Describe the morphology of the red blood cells.
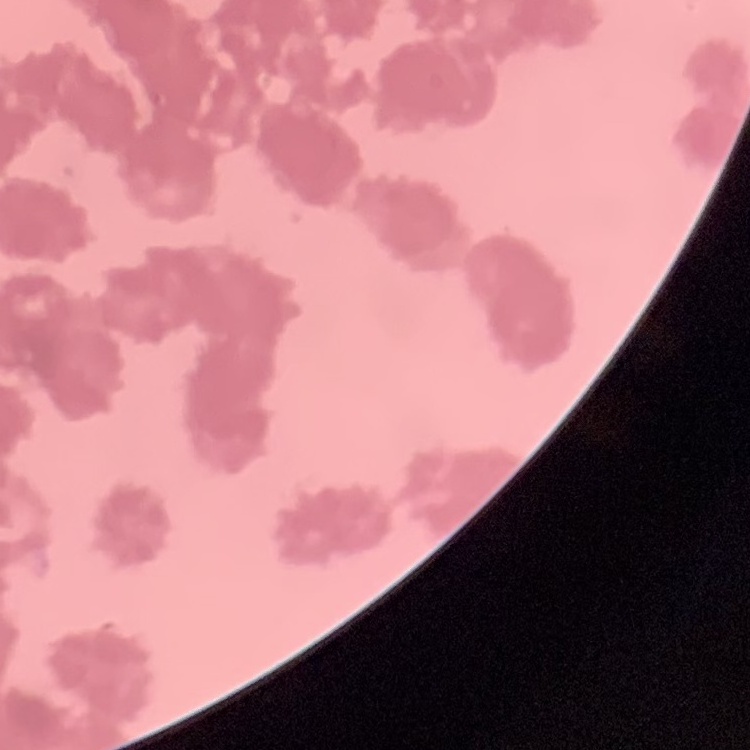

They show rouleaux formation.

Square crop of a larger photomicrograph. Thin peripheral smear. Field's or Giemsa stain.